Classify this cell by malaria status.
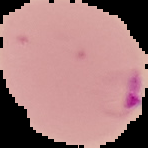
Parasitized.

image size = 148×148 pixels
image type = segmented cell region with the area outside set to black
preparation = thin blood film